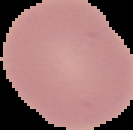

preparation = thin blood film
malaria status = uninfected
image type = segmented cell region with the area outside set to black
image size = 133×130 pixels